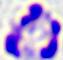
Summary:
  - Modality: photomicrograph
  - Identification: leukocyte
  - Magnification: 400x